State which parasite is depicted.
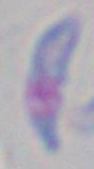

Toxoplasma gondii.

1000x magnification. Micrograph.